Point out each Plasmodium parasite.
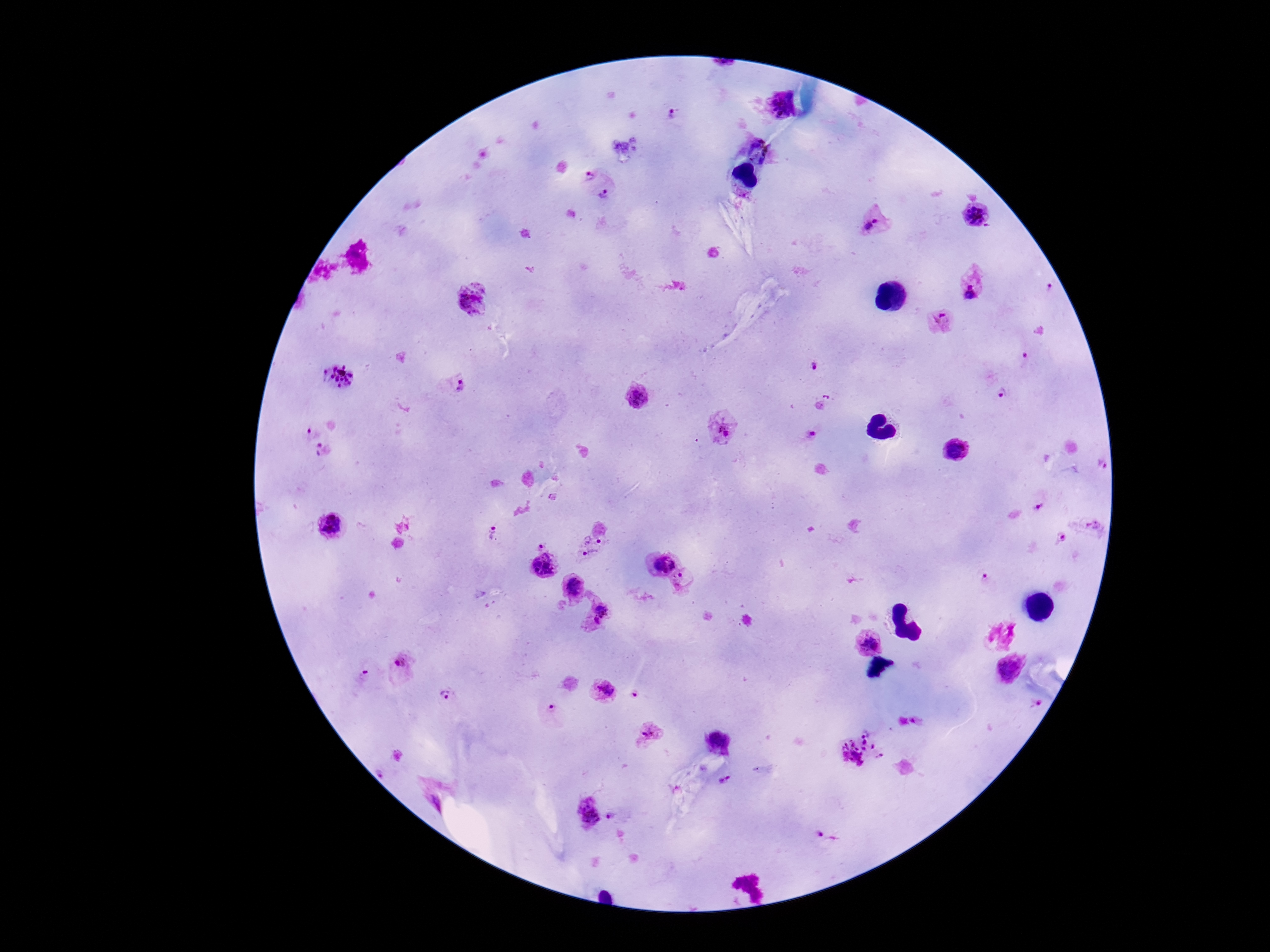

Approximate centers as [x, y] in pixels.
Plasmodium parasites: [779, 104], [672, 115], [758, 151], [592, 171], [609, 203], [976, 216], [876, 220], [971, 281], [475, 302], [941, 322], [1027, 357], [814, 366], [337, 377], [455, 385], [830, 393], [1002, 393], [638, 398], [724, 428], [312, 432], [813, 434], [955, 450], [325, 452], [1100, 464], [1038, 508], [1095, 524], [332, 527], [492, 534], [594, 538], [1061, 538], [541, 544], [590, 558], [659, 562], [546, 565], [983, 579], [682, 581], [572, 584], [601, 614], [867, 641], [1007, 671], [403, 672], [363, 679], [604, 690], [635, 695], [446, 699], [1039, 703], [550, 708], [649, 734], [719, 743], [861, 748], [726, 780], [435, 793], [588, 812], [614, 817].

preparation = thick peripheral-blood smear
capture = smartphone camera through the microscope eyepiece
image size = 1270×952 pixels
stain = Giemsa
magnification = 100x
patient malaria status = positive
field of view = one from this slide